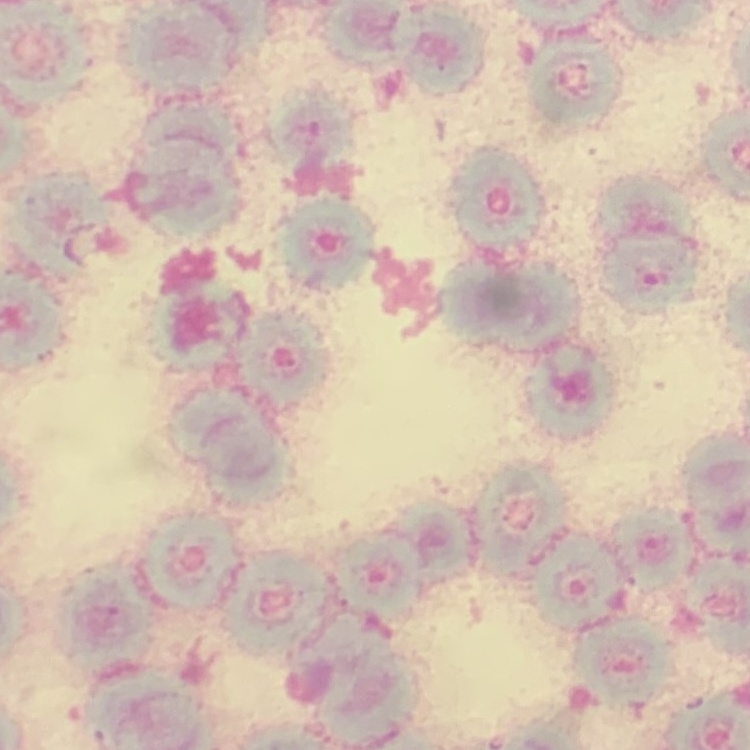
The erythrocytes show rouleaux formation. Thin blood film. Square crop of a larger photomicrograph. Stained with either Field's or Giemsa.